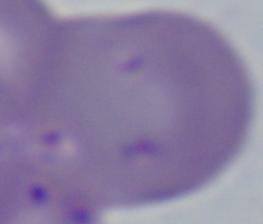
identification = Babesia
magnification = 1000x
modality = micrograph